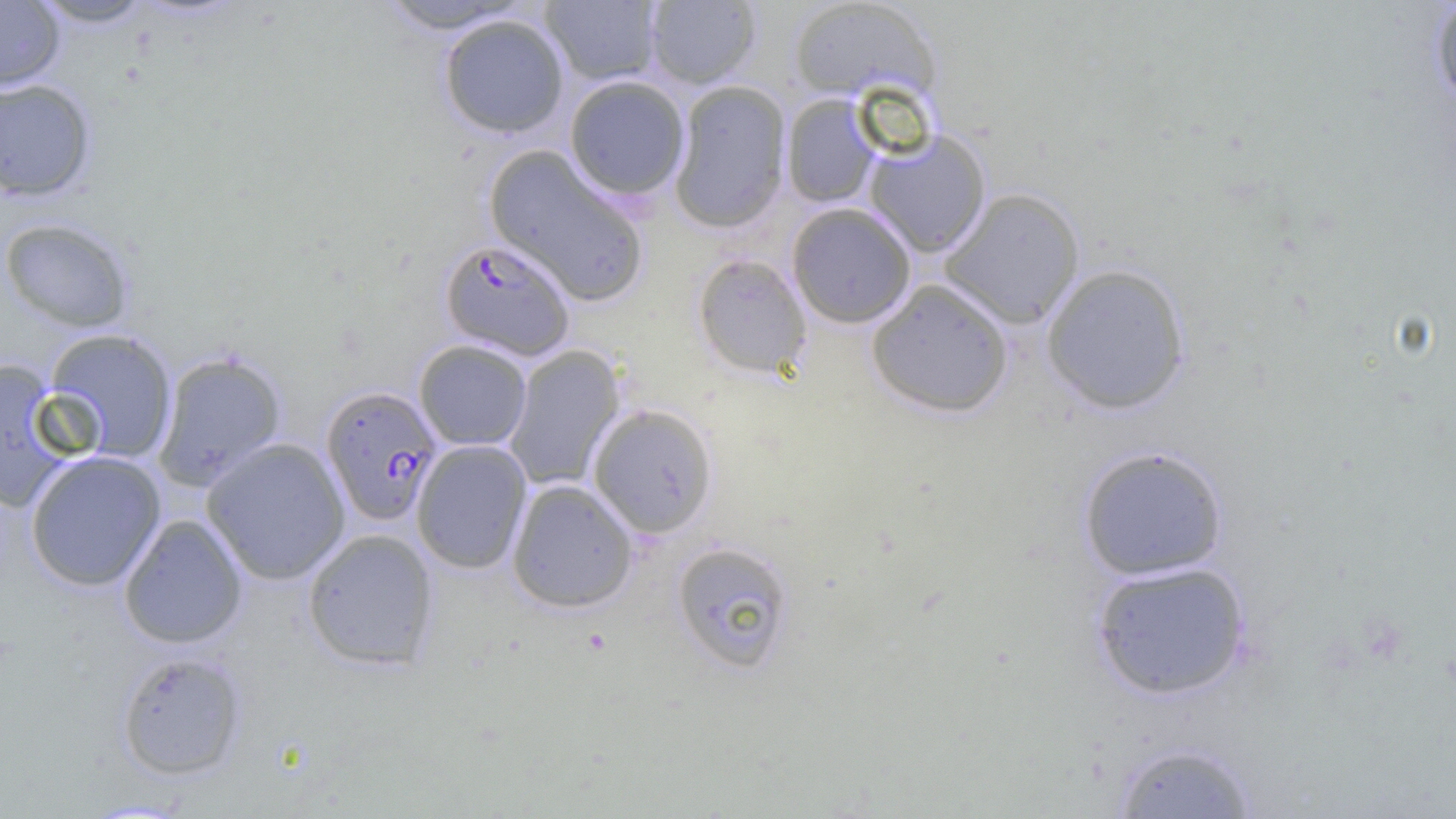
Plasmodium falciparum-infected red blood cell locations = approximate bounding boxes as (x1, y1, x2, y2) in pixels: (439, 238, 576, 360), (320, 386, 443, 525)
slide-level diagnosis = Plasmodium falciparum
uninfected red blood cell locations = approximate bounding boxes as (x1, y1, x2, y2) in pixels: (0, 0, 65, 92), (31, 0, 156, 28), (541, 0, 662, 85), (788, 0, 940, 102), (376, 1, 530, 34), (644, 1, 762, 88), (1429, 1, 1456, 112), (439, 14, 569, 138), (564, 75, 690, 201), (0, 78, 96, 202), (669, 80, 791, 233), (782, 94, 883, 208), (864, 129, 991, 258), (484, 145, 650, 307), (939, 188, 1085, 328), (787, 202, 916, 328), (0, 217, 135, 333), (692, 253, 812, 379), (1041, 263, 1191, 414), (866, 279, 1013, 418), (44, 328, 178, 463), (414, 340, 532, 451), (503, 345, 626, 491), (153, 350, 288, 490), (0, 358, 76, 514), (588, 404, 719, 538), (201, 437, 351, 585), (411, 440, 532, 573), (1077, 444, 1229, 581), (25, 450, 166, 591), (507, 479, 637, 612), (119, 514, 248, 649), (301, 528, 440, 671), (671, 540, 796, 674), (1090, 560, 1252, 700), (116, 651, 247, 780), (1110, 739, 1260, 818)
field of view = single
image size = 1456×819 pixels
preparation = thin blood film
magnification = 1000x
modality = optical microscopy